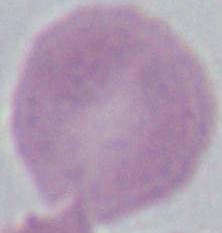
modality = photomicrograph
identification = erythrocyte
magnification = 1000x